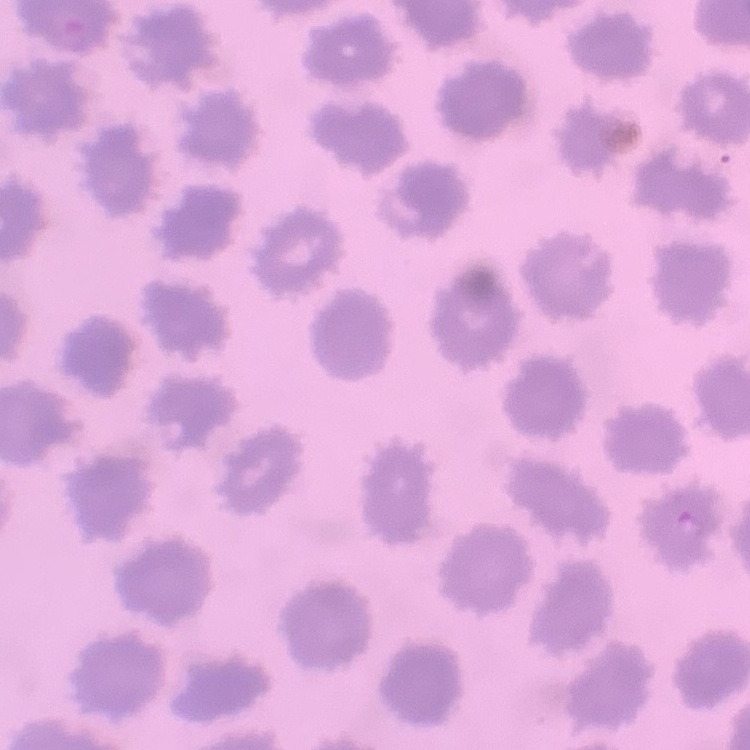 The erythrocytes exhibit no rouleaux formation. Thin blood film. Field's or Giemsa stain. Square crop of a larger photomicrograph.